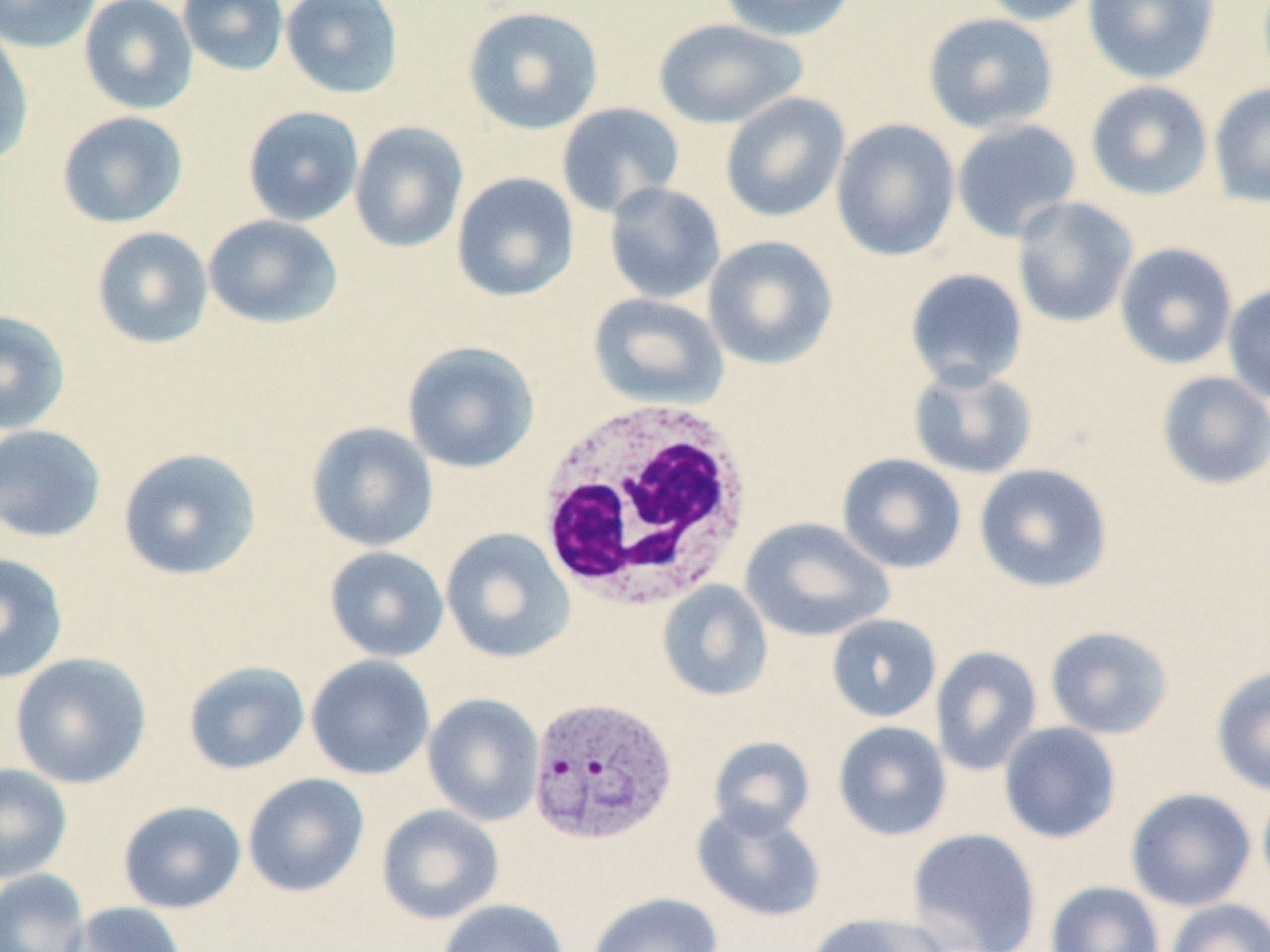

Approximate bounding boxes as (x1, y1, x2, y2) in pixels. Plasmodium vivax-infected red blood cell locations: (527, 695, 678, 846). Uninfected red blood cell locations: (0, 0, 103, 54), (79, 0, 199, 114), (177, 0, 289, 76), (279, 0, 405, 100), (717, 0, 860, 43), (978, 0, 1099, 26), (1082, 0, 1220, 85), (462, 4, 604, 134), (922, 13, 1058, 134), (652, 18, 807, 130), (0, 24, 35, 168), (1085, 80, 1213, 201), (1208, 83, 1270, 208), (720, 92, 851, 223), (556, 102, 684, 219), (242, 105, 364, 226), (56, 111, 189, 229), (830, 118, 961, 262), (951, 118, 1082, 244), (349, 121, 469, 253), (450, 172, 580, 303), (603, 181, 726, 305), (1012, 197, 1139, 329), (202, 214, 343, 331), (91, 226, 214, 349), (702, 235, 839, 371), (1114, 242, 1238, 370), (904, 268, 1029, 390), (1222, 282, 1270, 405), (588, 292, 729, 411), (0, 309, 71, 435), (401, 340, 540, 474), (907, 363, 1039, 480), (1155, 371, 1270, 490), (305, 421, 439, 552), (0, 424, 107, 544), (117, 446, 262, 581), (836, 453, 967, 574), (973, 463, 1114, 593), (739, 518, 894, 643), (440, 527, 576, 664), (324, 546, 449, 662), (0, 552, 68, 684), (656, 580, 773, 702), (826, 613, 942, 722), (1044, 625, 1174, 740), (931, 645, 1042, 776), (9, 652, 152, 789), (305, 654, 436, 780), (182, 660, 311, 775), (1210, 666, 1270, 796), (422, 693, 544, 826), (832, 720, 952, 841), (998, 721, 1122, 843), (708, 736, 815, 838), (0, 762, 73, 883), (242, 773, 369, 897), (1256, 782, 1270, 900), (1125, 787, 1256, 912), (117, 800, 246, 914), (692, 803, 826, 922), (376, 804, 504, 925), (906, 827, 1042, 952), (0, 868, 90, 952), (1045, 881, 1166, 952), (586, 891, 723, 952), (436, 898, 569, 952), (1165, 898, 1270, 952), (63, 902, 189, 952), (806, 912, 951, 952). White blood cell locations: (533, 397, 756, 612). Slide-level diagnosis: Plasmodium vivax. Light microscopy. Single field of view. May-Grünwald-Giemsa-stained preparation. 1000x magnification. Image is 1270×952 pixels. Thin blood smear.